Give the extent of all uninfected red blood cells.
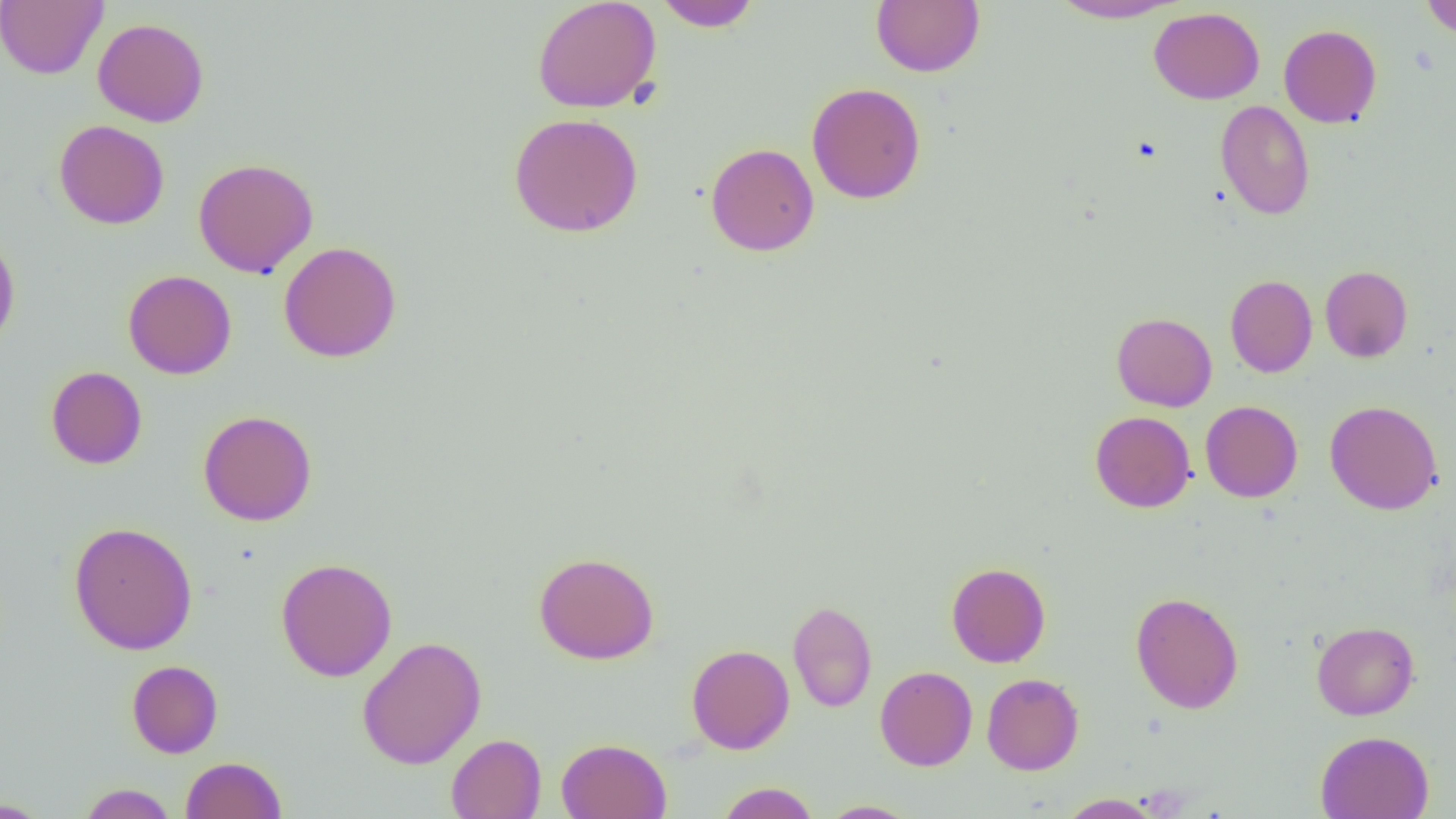

Approximate bounding boxes as (x1, y1, x2, y2) in pixels.
Uninfected red blood cells: (0, 0, 107, 79), (532, 0, 662, 113), (653, 0, 762, 31), (871, 0, 985, 77), (1048, 0, 1186, 23), (1420, 0, 1456, 40), (1149, 7, 1265, 104), (93, 18, 209, 127), (1278, 24, 1382, 128), (806, 82, 926, 204), (1215, 100, 1315, 220), (508, 112, 644, 237), (53, 120, 170, 229), (705, 142, 819, 256), (193, 157, 319, 278), (0, 234, 20, 351), (278, 241, 402, 362), (1320, 265, 1413, 362), (123, 270, 237, 379), (1225, 274, 1317, 378), (1112, 312, 1217, 411), (46, 366, 147, 469), (1200, 400, 1303, 503), (1325, 400, 1443, 515), (198, 410, 317, 526), (1090, 411, 1196, 512), (69, 521, 198, 655), (533, 552, 660, 664), (276, 557, 397, 682), (946, 562, 1051, 667), (1130, 591, 1244, 714), (787, 600, 877, 712), (1311, 621, 1419, 720), (356, 636, 487, 770), (686, 644, 794, 754), (127, 660, 223, 758), (875, 666, 977, 771), (982, 673, 1084, 775), (1315, 730, 1434, 819), (446, 733, 546, 818), (556, 738, 671, 819), (181, 756, 287, 819), (716, 782, 820, 819), (78, 783, 178, 818), (1056, 793, 1164, 818), (0, 798, 52, 818), (818, 800, 922, 818).

Slide-level diagnosis: no evidence of blood parasites. Thin blood smear. Captured at 1000x magnification. Optical microscopy. Image is 1456×819 pixels. One field of a larger specimen.